Look for Plasmodium parasites.
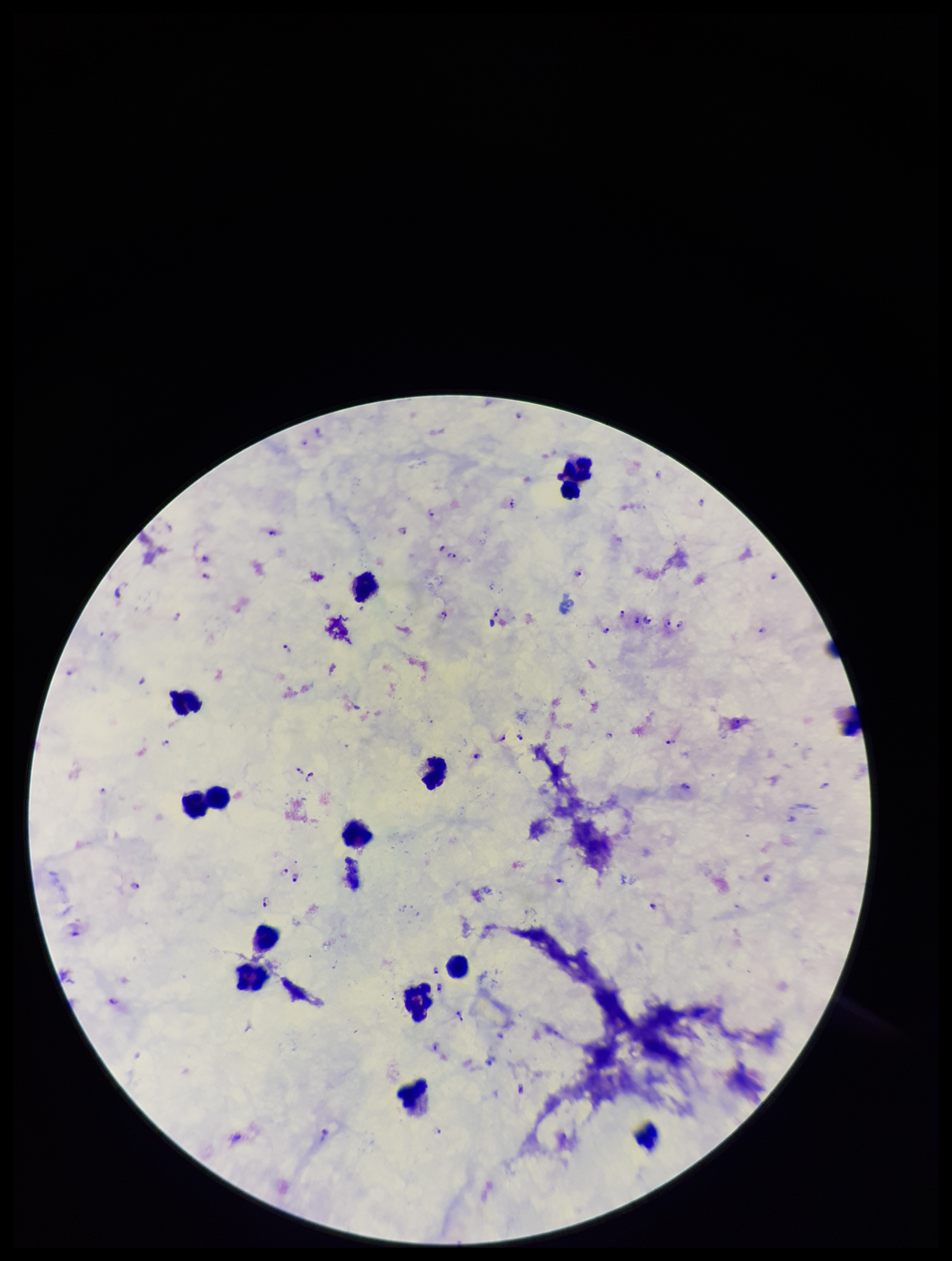
Identified.

stain = Giemsa
species reported for this patient = Plasmodium falciparum
patient malaria status = infected
leukocyte count = 13
image size = 952×1261 pixels
preparation = thick
parasite count = 37
field of view = one from this slide
capture = smartphone photograph through the microscope eyepiece